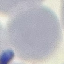 Result: no malaria parasites seen. Acquired by smartphone through the microscope eyepiece. Giemsa-stained preparation. Thin blood film. Cell patch, automatically extracted from a larger field of view and resized to 64 × 64 pixels.